Locate every blood parasite and identify its species.
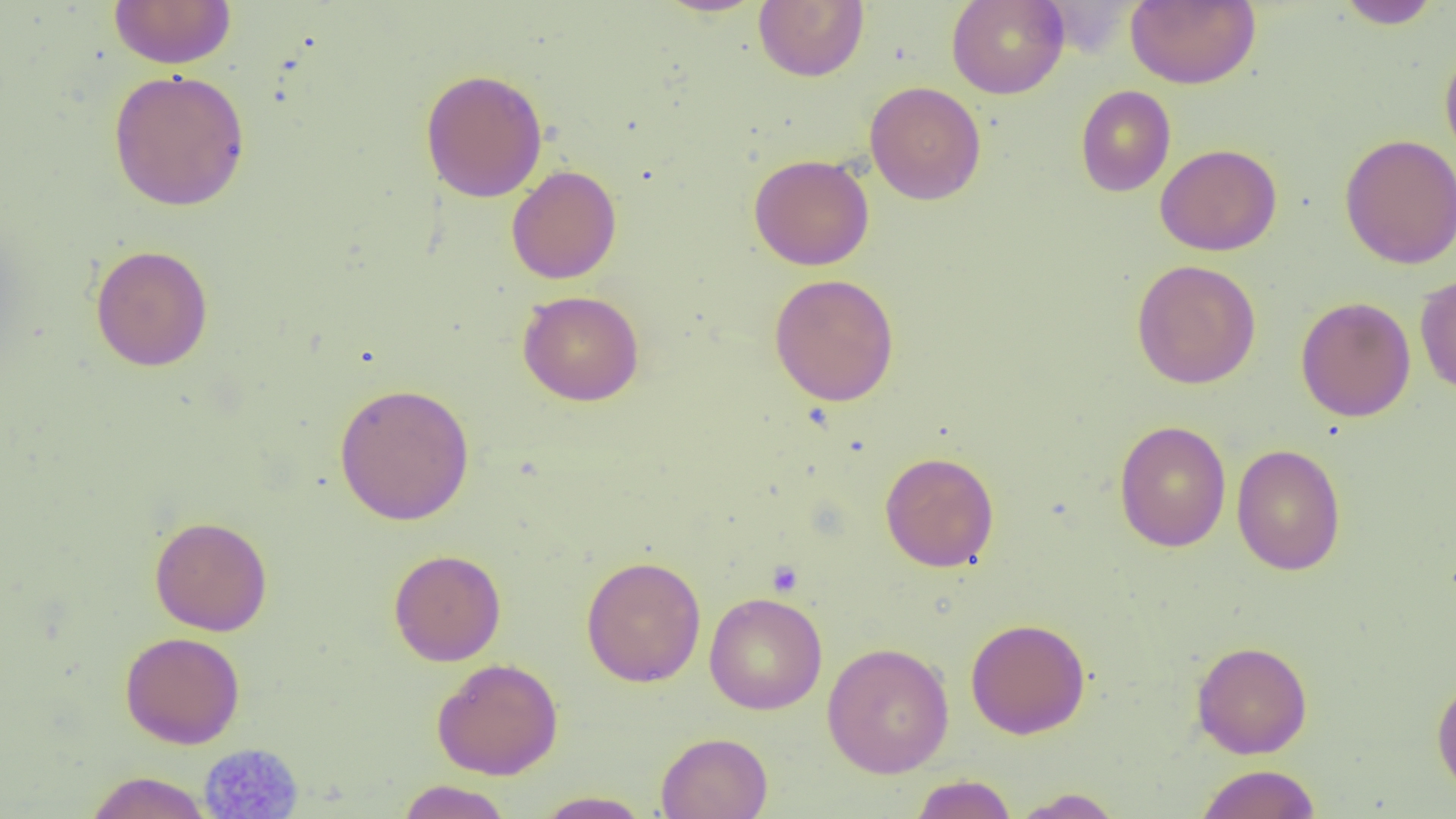

No blood parasites seen.

Approximate bounding boxes as [x1, y1, x2, y2] in pixels. Platelet locations (subset): [767, 561, 802, 596]. Uninfected red blood cell locations (subset): [108, 0, 236, 69], [653, 0, 768, 18], [946, 0, 1069, 99], [1125, 0, 1261, 89], [1335, 0, 1443, 29], [753, 1, 870, 82], [1440, 45, 1456, 168], [419, 68, 548, 203], [108, 69, 250, 211], [864, 81, 986, 205], [1075, 85, 1176, 197], [1338, 133, 1456, 270], [1155, 143, 1282, 256], [748, 154, 875, 270], [506, 165, 622, 284], [90, 244, 214, 371], [1131, 259, 1261, 389], [769, 274, 899, 406], [1415, 274, 1456, 396], [518, 290, 644, 406], [1295, 296, 1416, 422], [334, 382, 475, 526], [1114, 420, 1231, 552], [1231, 443, 1346, 576], [880, 451, 999, 572], [149, 516, 273, 636], [388, 549, 506, 666], [580, 555, 706, 688], [704, 592, 828, 715], [965, 618, 1091, 739], [120, 631, 245, 749], [1191, 640, 1313, 759], [822, 642, 955, 778], [432, 658, 563, 780], [1431, 677, 1456, 798], [656, 732, 773, 819], [1195, 764, 1321, 819], [85, 771, 213, 819], [909, 774, 1018, 819], [396, 780, 514, 819], [1008, 788, 1125, 818], [532, 790, 654, 818]. Slide-level diagnosis: negative for blood parasites. Image is 1456×819 pixels. Single field of view. Captured at 1000x magnification. Thin blood film. Optical microscopy.